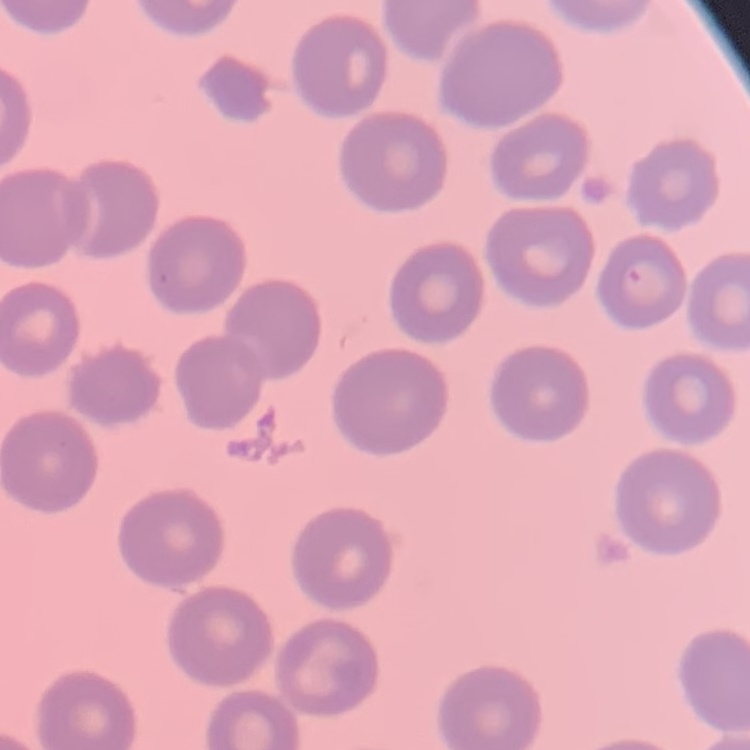
red_blood_cell_morphology: no rouleaux formation
preparation: thin peripheral smear
stain: Field's or Giemsa
image_type: square crop of a larger photomicrograph